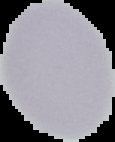

{
  "result": "negative for Plasmodium parasites",
  "preparation": "thin blood film",
  "image_type": "cell region segmented out of the field of view; surrounding area masked to black",
  "image_size": "115×142 pixels"
}